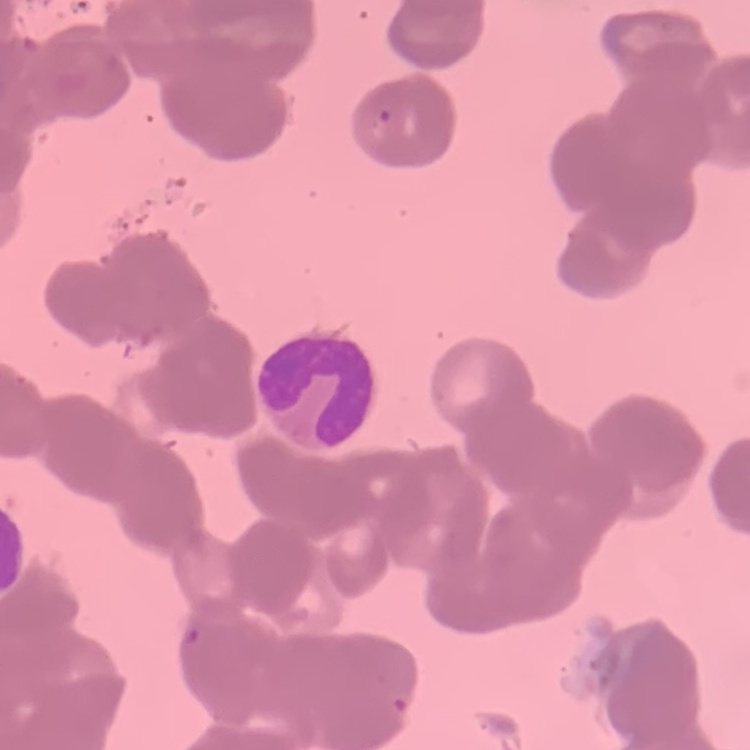
red blood cell morphology = rouleaux formation
stain = Field's or Giemsa
preparation = thin blood film
image type = square crop of a larger photomicrograph